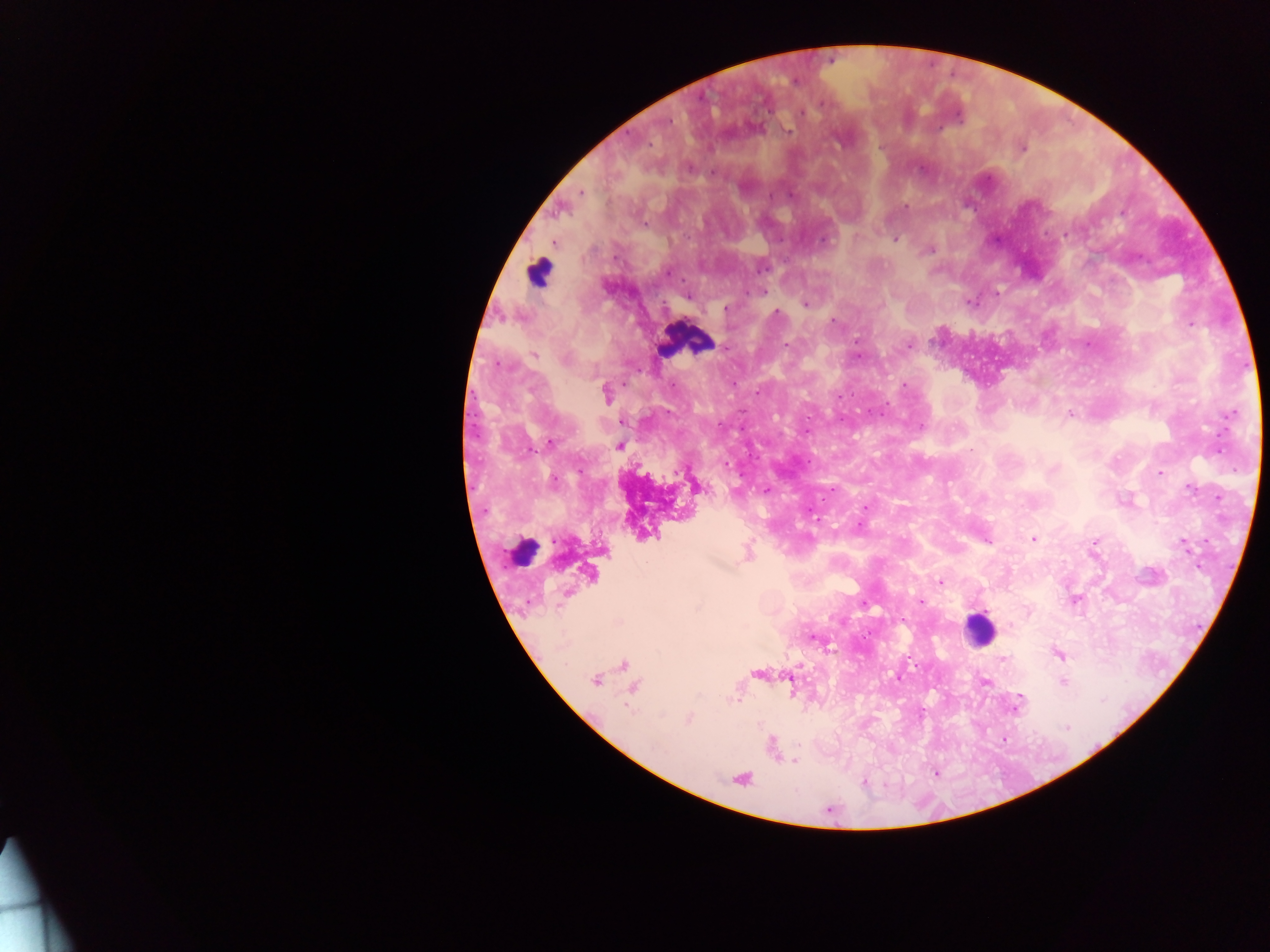 Approximate centers as {x, y} in pixels. Leukocyte locations: {539, 272}, {685, 340}, {523, 551}, {979, 630}. Plasmodium parasite locations: {795, 81}, {821, 104}, {802, 113}, {668, 122}, {788, 132}, {879, 147}, {1021, 148}, {689, 167}, {922, 169}, {712, 172}, {581, 192}, {771, 196}, {791, 196}, {906, 207}, {646, 223}, {824, 240}, {894, 240}, {929, 250}, {764, 291}, {997, 293}, {687, 296}, {968, 302}, {805, 303}, {726, 308}, {777, 313}, {833, 319}, {1190, 325}, {857, 341}, {786, 345}, {908, 345}, {723, 347}, {534, 356}, {565, 359}, {500, 365}, {905, 385}, {758, 392}, {606, 394}, {840, 397}, {883, 412}, {1070, 414}, {1232, 415}, {920, 426}, {807, 432}, {550, 443}, {619, 446}, {971, 449}, {726, 465}, {1160, 473}, {553, 480}, {1191, 488}, {832, 489}, {766, 491}, {865, 507}, {860, 526}, {1034, 539}, {987, 541}, {1184, 544}, {940, 583}, {920, 601}, {1075, 601}, {864, 604}, {902, 621}, {812, 638}, {1059, 654}, {1003, 659}, {595, 681}, {1063, 682}, {986, 683}, {1019, 702}, {688, 719}, {1067, 728}, {794, 761}, {863, 782}. Mobile-phone photograph taken through the microscope. Sample from Ghana. Image is 1270×952 pixels. Thick blood film. One field of view.